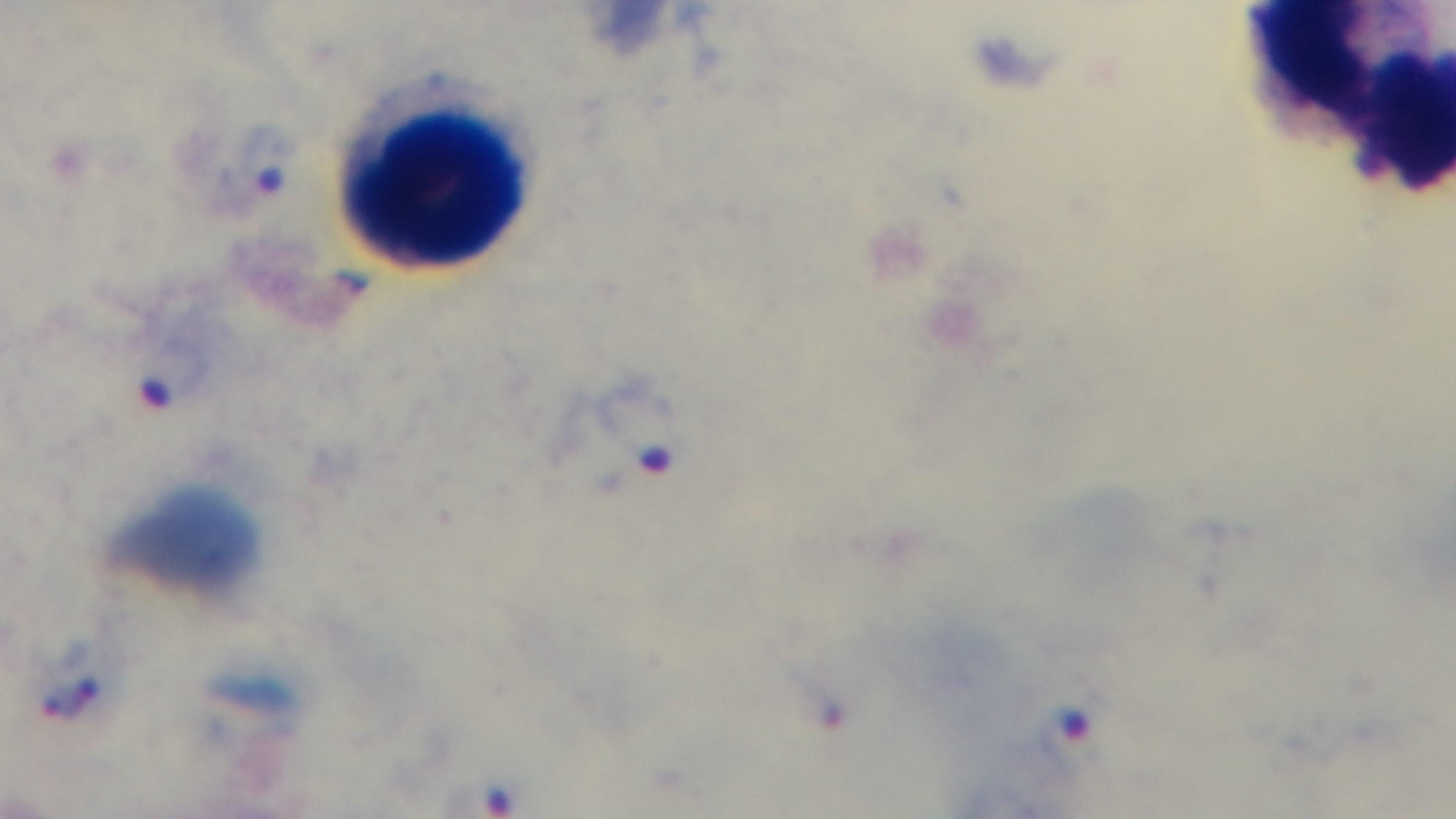

Single field of view. Giemsa stain. Malaria status: positive. Captured with a mounted 4K digital camera. 100x oil-immersion objective. Photomicrograph. Preparation: thick.